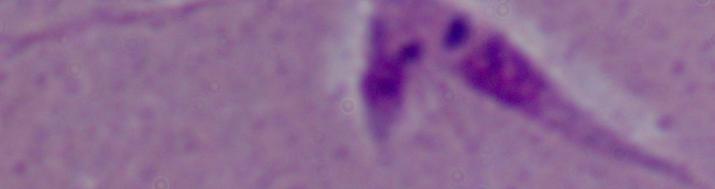
Summary:
  - Modality: micrograph
  - Magnification: 1000x
  - Identification: Leishmania